State which parasite is depicted.
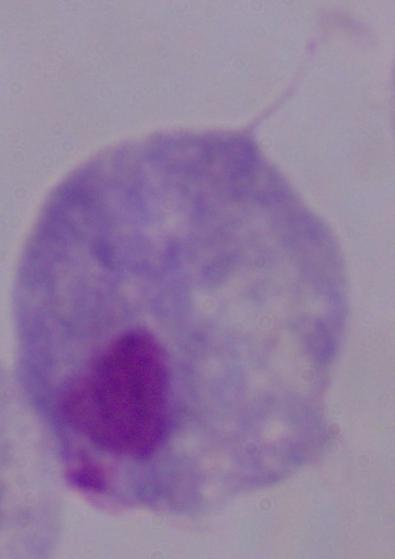
A trichomonad.

magnification = 1000x
modality = photomicrograph